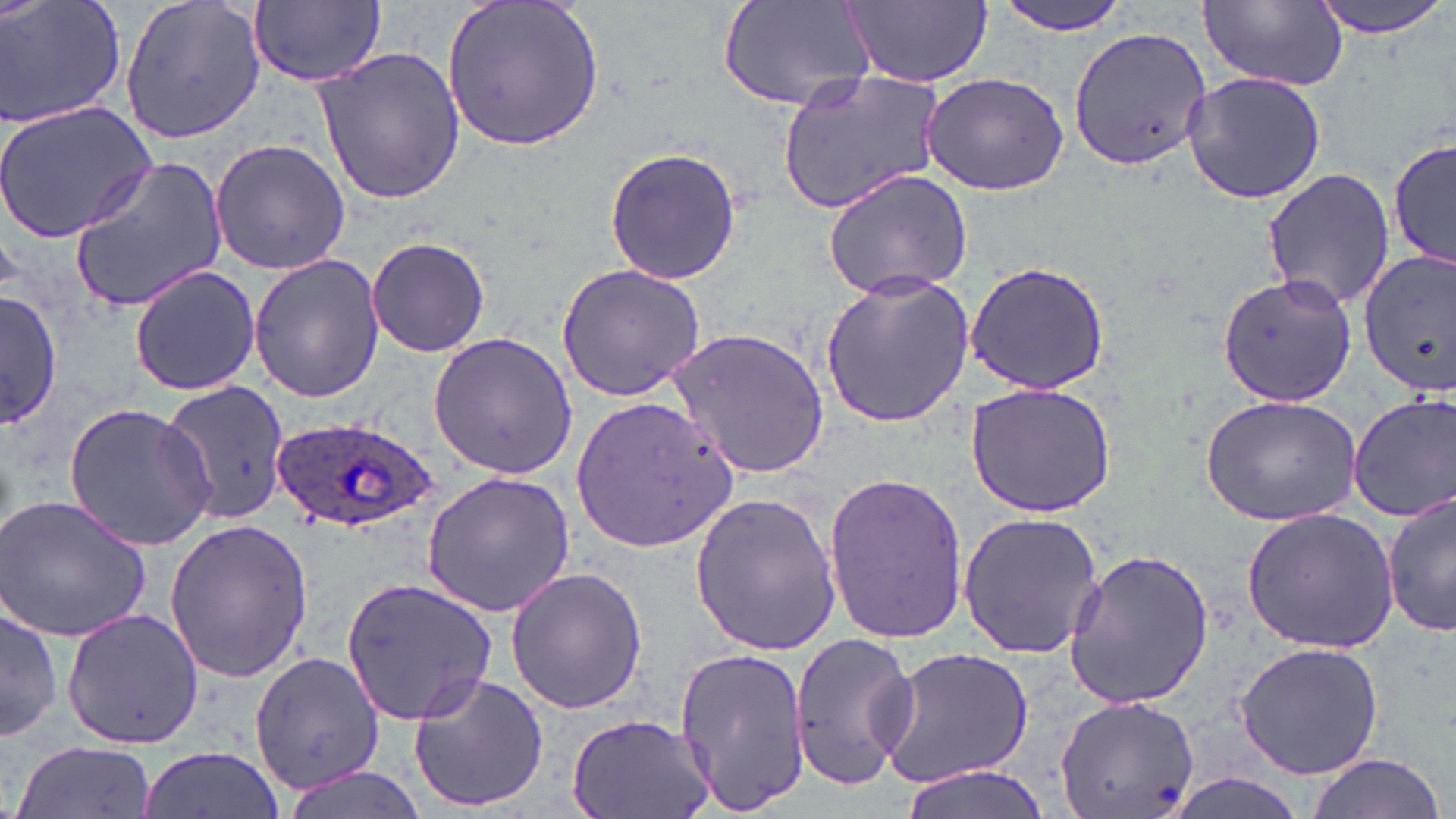

Summary:
  - Coordinate format: approximate bounding boxes as named x1/y1/x2/y2 corners in pixels
  - Uninfected red blood cell locations: (x1=0, y1=0, x2=125, y2=130), (x1=117, y1=0, x2=268, y2=146), (x1=439, y1=0, x2=606, y2=154), (x1=721, y1=0, x2=878, y2=115), (x1=992, y1=0, x2=1138, y2=36), (x1=1308, y1=0, x2=1452, y2=38), (x1=248, y1=1, x2=386, y2=87), (x1=841, y1=1, x2=991, y2=87), (x1=1198, y1=1, x2=1347, y2=91), (x1=1066, y1=27, x2=1214, y2=172), (x1=312, y1=47, x2=467, y2=205), (x1=777, y1=69, x2=949, y2=212), (x1=1181, y1=70, x2=1326, y2=206), (x1=921, y1=71, x2=1069, y2=196), (x1=0, y1=100, x2=158, y2=243), (x1=1388, y1=130, x2=1455, y2=276), (x1=210, y1=138, x2=350, y2=276), (x1=602, y1=146, x2=743, y2=286), (x1=65, y1=154, x2=231, y2=312), (x1=1261, y1=167, x2=1395, y2=311), (x1=823, y1=168, x2=977, y2=300), (x1=364, y1=237, x2=491, y2=355), (x1=1356, y1=249, x2=1455, y2=396), (x1=249, y1=253, x2=386, y2=403), (x1=964, y1=259, x2=1113, y2=395), (x1=556, y1=263, x2=706, y2=400), (x1=127, y1=265, x2=262, y2=395), (x1=818, y1=272, x2=976, y2=429), (x1=1217, y1=273, x2=1356, y2=407), (x1=2, y1=289, x2=62, y2=431), (x1=667, y1=326, x2=829, y2=478), (x1=426, y1=331, x2=579, y2=480), (x1=154, y1=381, x2=293, y2=532), (x1=965, y1=382, x2=1118, y2=516), (x1=1349, y1=391, x2=1456, y2=523), (x1=1201, y1=393, x2=1364, y2=526), (x1=572, y1=396, x2=738, y2=552), (x1=64, y1=402, x2=218, y2=551), (x1=422, y1=472, x2=574, y2=618), (x1=822, y1=472, x2=970, y2=646), (x1=1383, y1=487, x2=1455, y2=641), (x1=688, y1=492, x2=842, y2=658), (x1=0, y1=494, x2=153, y2=644), (x1=1241, y1=508, x2=1400, y2=653), (x1=957, y1=512, x2=1105, y2=658), (x1=163, y1=518, x2=313, y2=684), (x1=1062, y1=546, x2=1215, y2=709), (x1=503, y1=565, x2=647, y2=713), (x1=342, y1=577, x2=498, y2=725), (x1=1, y1=600, x2=61, y2=744), (x1=63, y1=608, x2=204, y2=748), (x1=789, y1=631, x2=920, y2=790), (x1=1235, y1=641, x2=1385, y2=779), (x1=873, y1=644, x2=1037, y2=791), (x1=672, y1=646, x2=811, y2=818), (x1=250, y1=649, x2=383, y2=793), (x1=408, y1=674, x2=550, y2=812), (x1=1052, y1=694, x2=1200, y2=819), (x1=566, y1=713, x2=716, y2=819), (x1=11, y1=738, x2=154, y2=817), (x1=137, y1=746, x2=285, y2=819), (x1=1302, y1=752, x2=1443, y2=819), (x1=277, y1=764, x2=427, y2=819), (x1=892, y1=766, x2=1053, y2=819)
  - Plasmodium ovale-infected red blood cell locations: (x1=271, y1=416, x2=439, y2=537)
  - Slide-level diagnosis: Plasmodium ovale
  - Field of view: one of a larger specimen
  - Preparation: thin blood smear
  - Magnification: 1000x
  - Stain: May-Grünwald-Giemsa
  - Modality: light microscopy
  - Image size: 1456×819 pixels